Assess this cell for malaria.
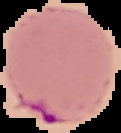
It is parasitized.

image size = 121×133 pixels
preparation = thin blood film
image type = cell region segmented out of the field of view; surrounding area masked to black